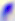

magnification = 400x
modality = micrograph
identification = Toxoplasma gondii